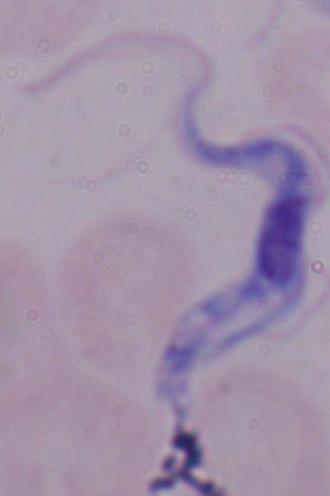
A trypanosome is shown. Micrograph. 1000x magnification.